Identify the parasite.
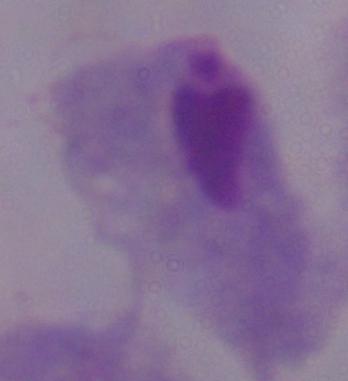
A trichomonad.

Micrograph. 1000x magnification.